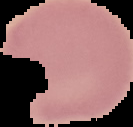

Cell region segmented out of the field of view; the surrounding area is masked to black. From a thin blood film. Image is 133×127 pixels. Malaria status: uninfected.